Give the extent of all Plasmodium parasites.
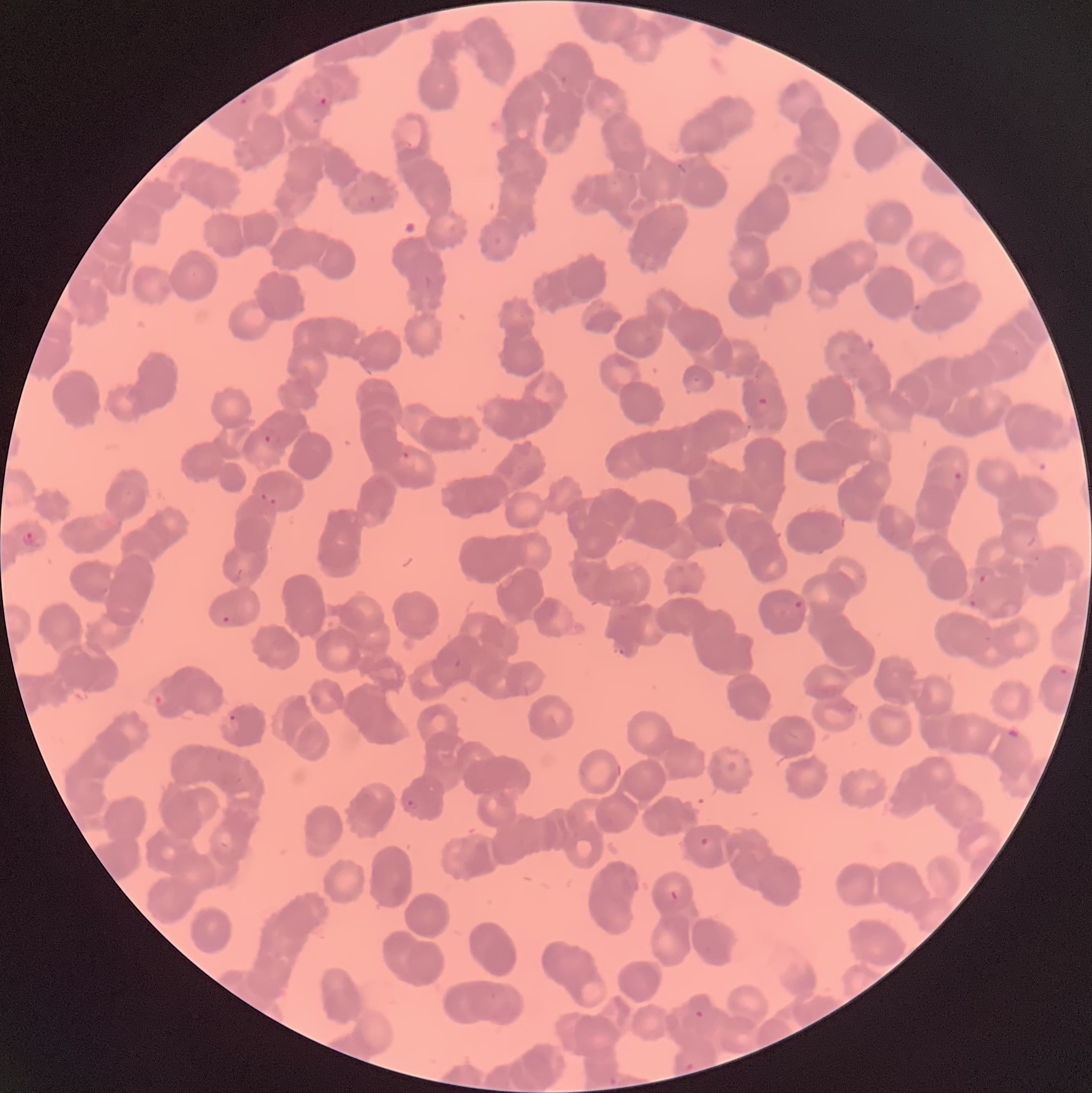

Approximate bounding boxes as (x1,y1)-(x2,y2) corner pairs in pixels.
Plasmodium parasites: (238,96)-(250,105), (318,97)-(328,106), (753,397)-(771,415), (262,432)-(281,445), (402,451)-(414,461), (952,469)-(964,482), (259,491)-(280,505), (21,531)-(39,546), (977,572)-(992,585), (793,599)-(804,611), (968,599)-(978,610), (222,615)-(231,624), (453,657)-(463,670), (1057,667)-(1072,678), (227,713)-(238,725), (405,799)-(419,809), (699,836)-(714,851), (668,889)-(679,901), (690,995)-(711,1018), (685,1062)-(696,1071), (607,1075)-(618,1087).

preparation = thin blood smear
red blood cell morphology = rouleaux formation
image size = 1092×1093 pixels
modality = optical microscopy